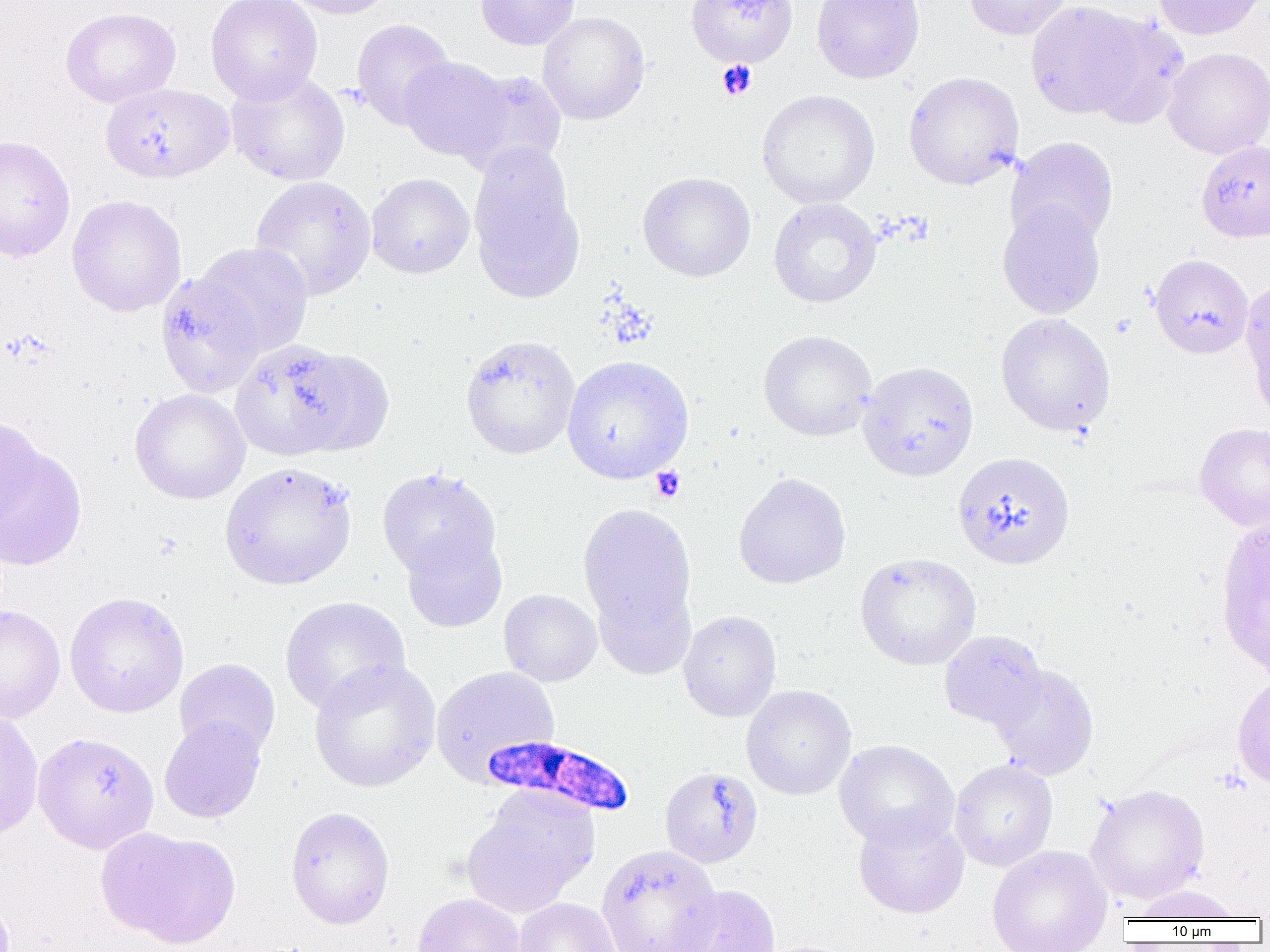
slide-level diagnosis = Plasmodium falciparum
magnification = 1000x
uninfected red blood cell locations = approximate bounding boxes as [x1, y1, x2, y2] in pixels: [206, 0, 323, 104], [278, 0, 400, 19], [475, 0, 581, 50], [685, 0, 798, 68], [812, 0, 925, 83], [963, 0, 1072, 40], [1152, 0, 1267, 40], [1026, 1, 1146, 120], [61, 6, 181, 108], [537, 11, 650, 124], [1083, 13, 1189, 130], [351, 19, 456, 129], [1163, 47, 1270, 159], [399, 57, 511, 162], [458, 70, 567, 177], [226, 71, 350, 186], [903, 71, 1024, 190], [100, 83, 234, 183], [757, 89, 880, 209], [0, 135, 75, 263], [1006, 136, 1119, 248], [1196, 140, 1270, 242], [468, 146, 584, 303], [638, 171, 756, 281], [367, 173, 474, 279], [250, 175, 377, 301], [66, 195, 187, 317], [768, 198, 882, 308], [997, 201, 1106, 319], [193, 242, 313, 357], [1149, 254, 1253, 358], [155, 273, 265, 400], [1240, 275, 1270, 415], [995, 312, 1116, 436], [758, 330, 877, 441], [460, 335, 581, 459], [230, 340, 360, 460], [290, 347, 395, 458], [561, 355, 694, 484], [857, 361, 979, 481], [129, 389, 250, 504], [0, 415, 43, 533], [1194, 422, 1270, 532], [0, 443, 87, 571], [952, 451, 1075, 570], [219, 461, 357, 591], [377, 468, 501, 581], [733, 472, 851, 589], [578, 503, 697, 642], [1215, 513, 1269, 680], [401, 528, 507, 632], [855, 552, 982, 670], [591, 578, 697, 680], [498, 589, 602, 686], [64, 591, 189, 718], [279, 596, 411, 714], [0, 604, 66, 723], [678, 610, 781, 723], [939, 630, 1047, 730], [174, 658, 281, 760], [309, 658, 441, 793], [991, 664, 1099, 779], [430, 666, 560, 783], [1232, 673, 1270, 790], [741, 685, 856, 800], [0, 707, 44, 840], [159, 715, 267, 823], [33, 731, 159, 853], [834, 739, 959, 850], [949, 759, 1058, 871], [660, 767, 763, 868], [1085, 784, 1210, 904], [460, 791, 598, 919], [285, 806, 395, 929], [854, 812, 969, 919], [95, 827, 240, 950], [596, 845, 722, 952], [987, 845, 1114, 952], [671, 884, 782, 952], [1129, 884, 1246, 921], [412, 892, 528, 952], [514, 898, 622, 952]
Plasmodium falciparum-infected red blood cell locations = approximate bounding boxes as [x1, y1, x2, y2] in pixels: [474, 732, 630, 818]
image size = 1270×952 pixels
modality = light microscopy
platelet locations = approximate bounding boxes as [x1, y1, x2, y2] in pixels: [717, 60, 757, 100], [650, 466, 685, 503]
preparation = thin blood film
field of view = one of a larger specimen